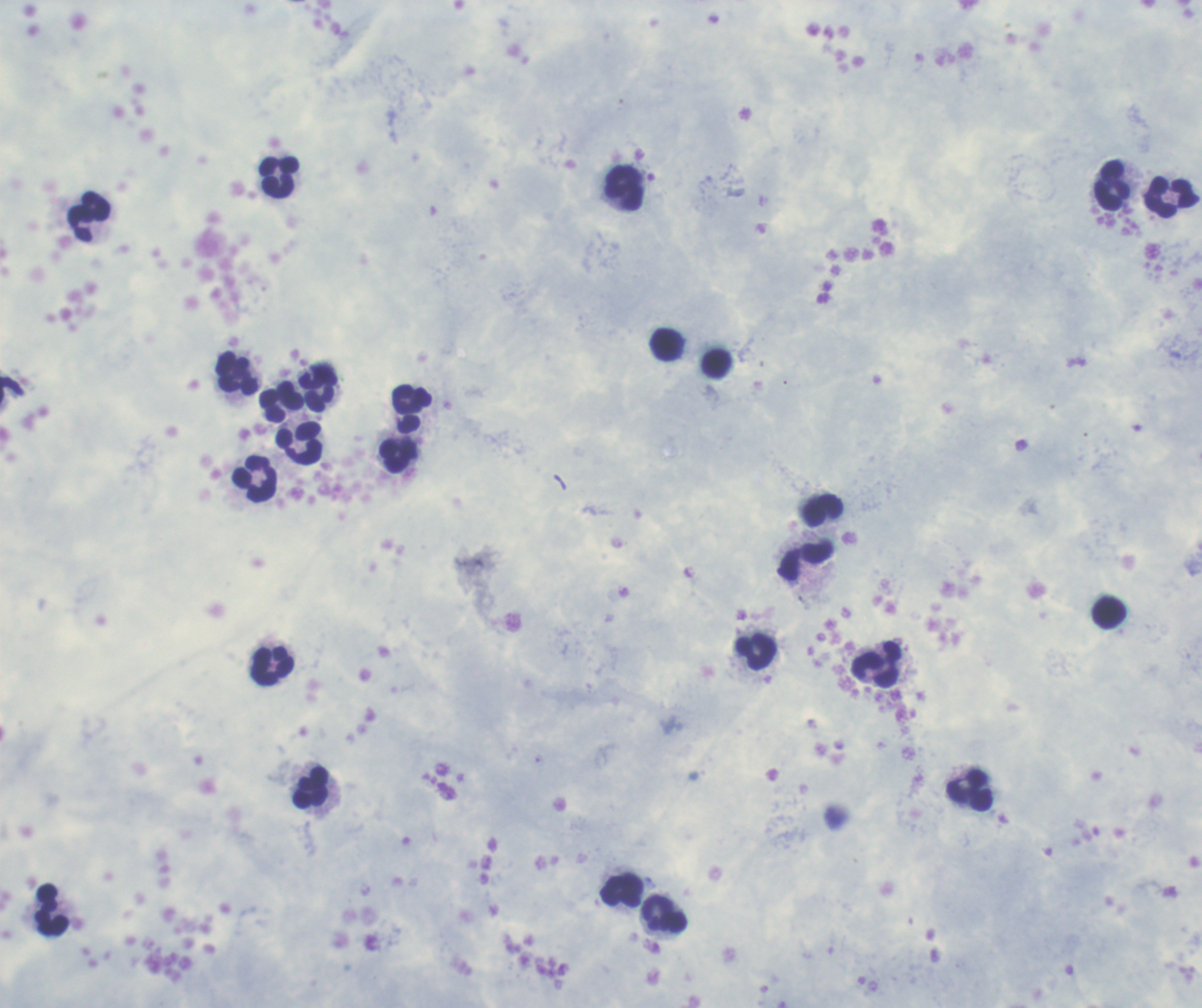
Coloration quality: good. One field from this slide. Romanowsky stain. Image is 1202×1008 pixels. Thick blood smear.